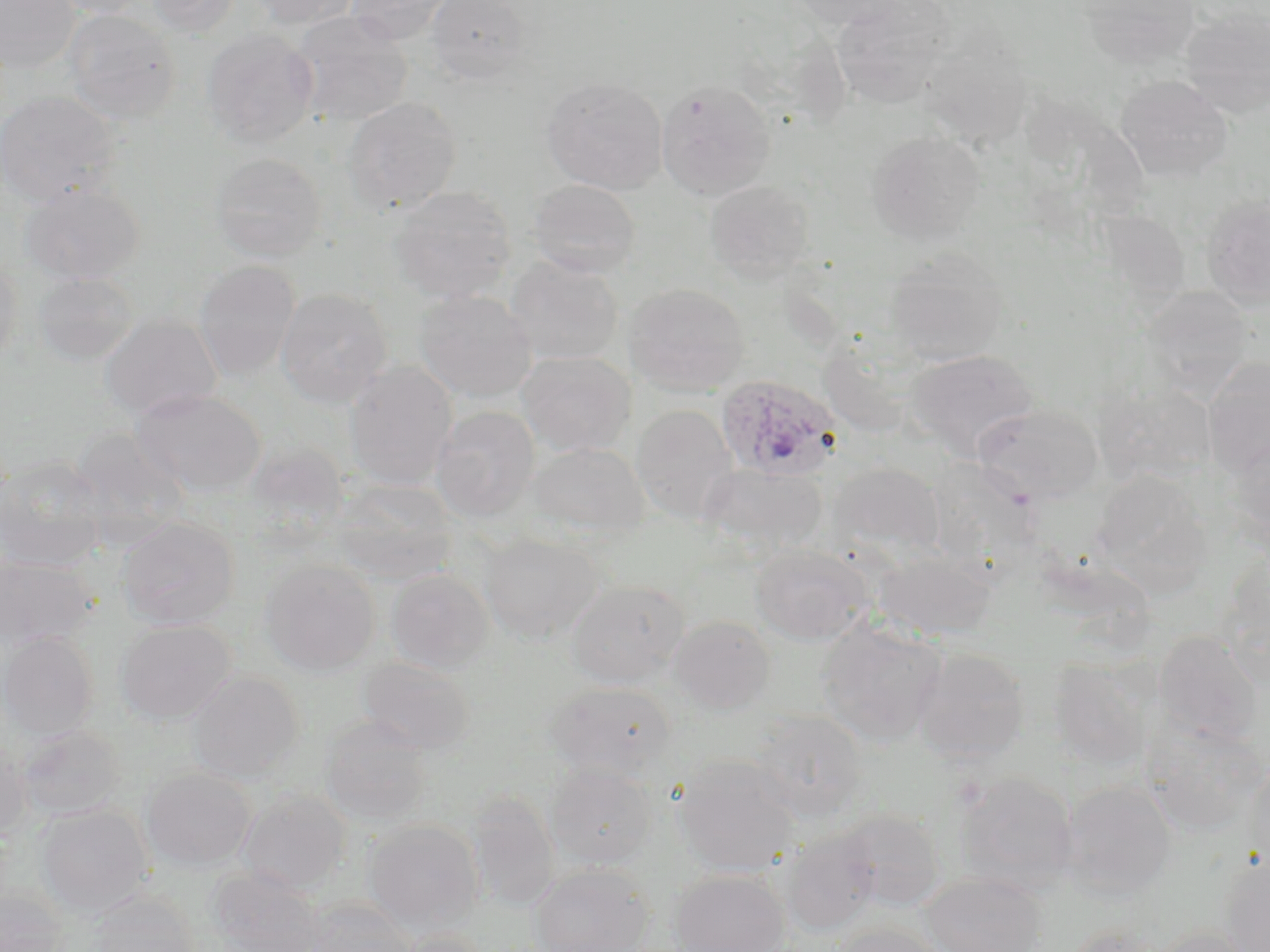
Approximate bounding boxes as [x1, y1, x2, y2] in pixels. Uninfected red blood cell locations: [0, 0, 81, 73], [46, 0, 155, 19], [144, 0, 244, 36], [246, 0, 360, 29], [345, 0, 457, 46], [424, 0, 534, 84], [787, 0, 906, 29], [832, 1, 954, 109], [1079, 1, 1200, 70], [1, 3, 140, 100], [1180, 8, 1270, 117], [62, 9, 181, 124], [292, 12, 413, 126], [201, 28, 318, 148], [918, 33, 1034, 149], [1115, 75, 1233, 183], [541, 77, 669, 195], [655, 79, 776, 200], [0, 90, 121, 208], [343, 97, 462, 215], [866, 130, 984, 244], [210, 152, 326, 262], [527, 179, 641, 278], [704, 180, 816, 283], [19, 181, 145, 285], [390, 185, 517, 304], [1201, 196, 1269, 309], [884, 247, 1009, 366], [0, 255, 23, 369], [505, 255, 624, 366], [194, 260, 301, 381], [33, 272, 138, 366], [624, 282, 750, 396], [276, 287, 393, 407], [1142, 287, 1252, 400], [414, 290, 537, 403], [99, 314, 223, 421], [816, 338, 929, 440], [905, 349, 1039, 460], [516, 351, 636, 457], [1202, 356, 1270, 475], [344, 361, 458, 491], [1094, 381, 1215, 485], [130, 388, 265, 496], [975, 403, 1103, 505], [631, 404, 739, 525], [432, 406, 540, 521], [69, 428, 191, 546], [1227, 436, 1270, 551], [245, 441, 349, 537], [529, 442, 650, 540], [0, 456, 110, 571], [826, 462, 945, 565], [704, 464, 828, 557], [1091, 471, 1210, 596], [332, 478, 456, 583], [117, 515, 240, 630], [480, 531, 603, 644], [750, 543, 873, 645], [874, 550, 995, 639], [1217, 554, 1270, 686], [0, 555, 98, 652], [260, 558, 380, 675], [385, 568, 495, 674], [565, 579, 690, 688], [667, 614, 776, 714], [115, 619, 236, 724], [815, 619, 947, 746], [1152, 630, 1263, 745], [1, 633, 98, 739], [913, 647, 1030, 763], [357, 656, 476, 754], [1048, 659, 1156, 769], [186, 670, 304, 783], [545, 682, 678, 781], [747, 709, 870, 823], [320, 715, 433, 827], [15, 723, 126, 820], [1142, 724, 1268, 835], [0, 737, 32, 841], [673, 755, 800, 877], [1246, 755, 1270, 872], [545, 761, 658, 868], [142, 767, 256, 871], [954, 771, 1078, 894], [1059, 779, 1178, 900], [237, 789, 351, 894], [468, 791, 560, 913], [35, 805, 153, 918], [835, 808, 946, 911], [362, 819, 484, 932], [781, 830, 879, 937], [1218, 853, 1270, 952], [529, 863, 655, 951], [207, 867, 325, 952], [669, 869, 790, 951], [922, 872, 1048, 952], [0, 888, 68, 951], [89, 892, 200, 952], [301, 898, 418, 952], [830, 922, 945, 951], [1066, 922, 1164, 952], [1149, 925, 1256, 952], [396, 928, 490, 952]. Plasmodium ovale-infected red blood cell locations: [715, 373, 844, 482]. Slide-level diagnosis: Plasmodium ovale. Single field of view. Thin blood film. Light microscopy. May-Grünwald-Giemsa-stained preparation. Captured at 1000x magnification. Image is 1270×952 pixels.